Give the preparation type.
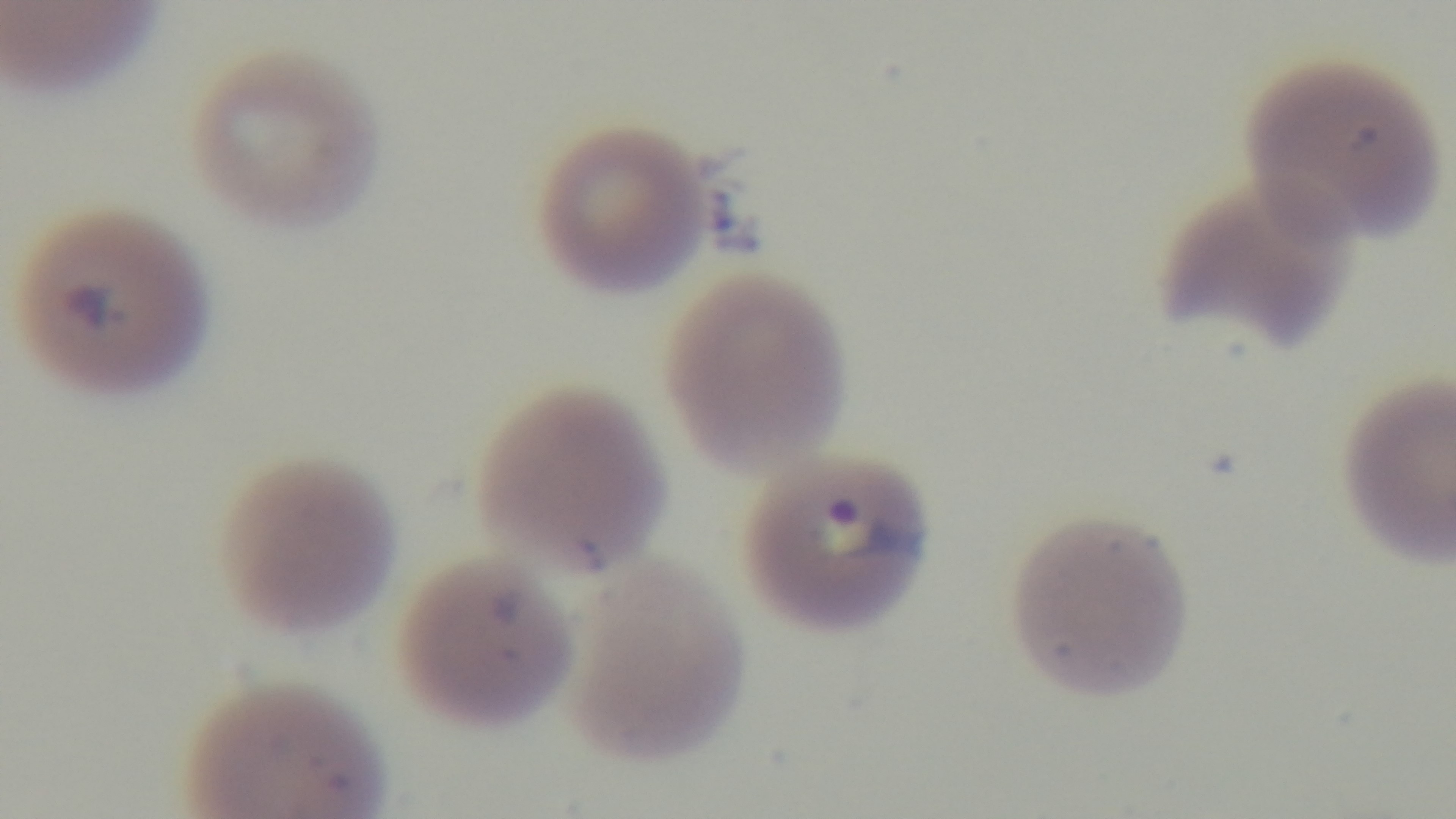

Thin.

Giemsa-stained. Light microscopy. Captured with a mounted 4K digital camera. Oil-immersion objective, 100x. Malaria status: infected. One field from the slide.